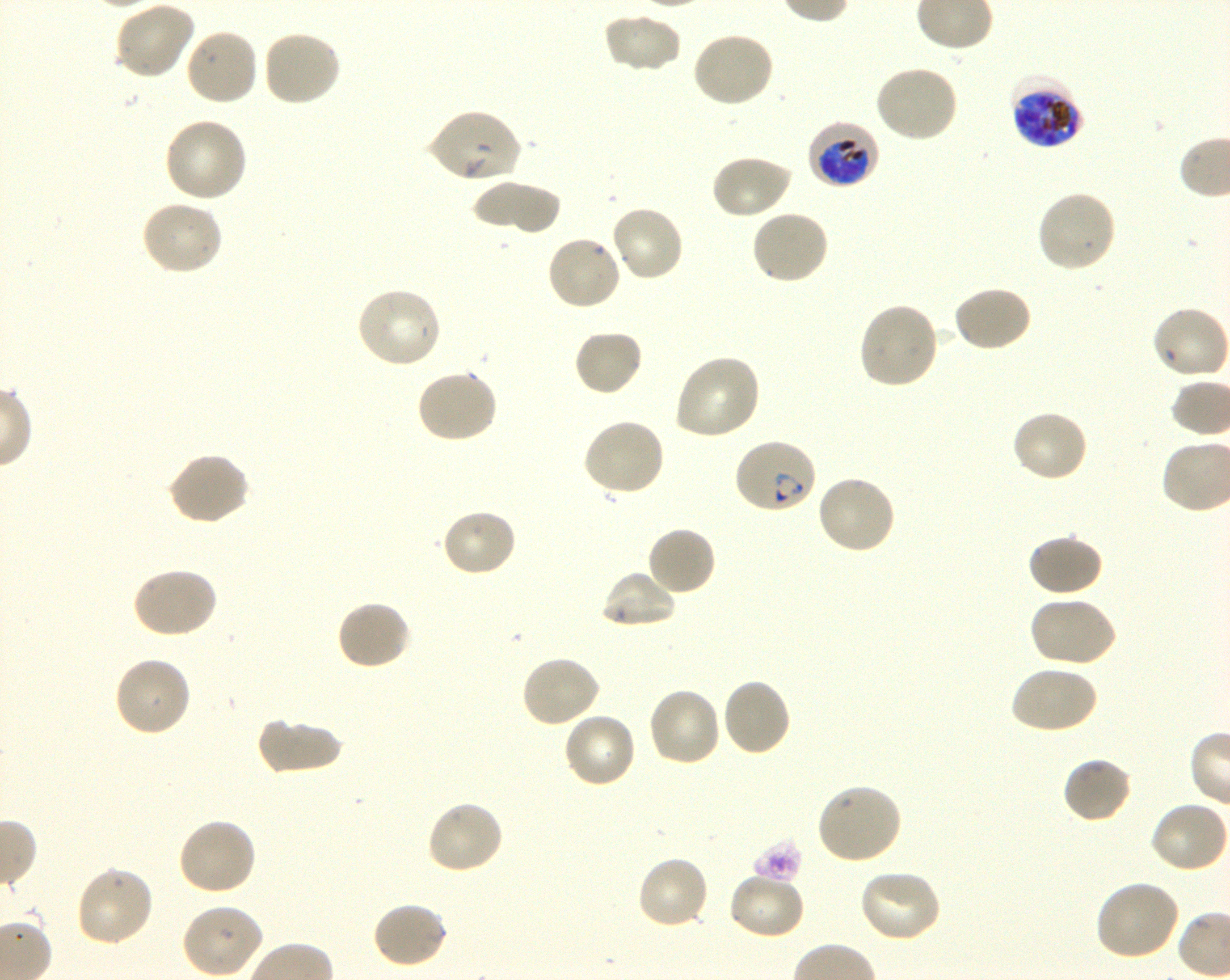

Approximate bounding boxes as [x1, y1, x2, y2] in pixels. Not every red blood cell is marked. A life-cycle stage — or a range of stages, where the recorded stages span more than one — follows each staged infected red blood cell.
Summary:
  - Locations of red blood cells of indeterminate infection status: [426, 109, 522, 185]
  - Locations of uninfected red blood cells: [113, 1, 195, 81], [602, 12, 682, 74], [183, 27, 259, 107], [261, 28, 342, 108], [690, 31, 775, 109], [873, 63, 959, 143], [164, 117, 249, 203], [709, 153, 792, 220], [470, 181, 562, 234], [1035, 188, 1118, 275], [139, 199, 224, 276], [609, 204, 685, 283], [750, 209, 830, 285], [545, 233, 623, 312], [952, 284, 1033, 353], [354, 286, 444, 369], [856, 301, 939, 391], [1150, 305, 1229, 381], [573, 328, 644, 397], [673, 353, 762, 441], [415, 368, 498, 444], [1011, 409, 1089, 484], [581, 417, 666, 497], [167, 452, 252, 527], [816, 473, 898, 555], [440, 508, 518, 579], [645, 525, 717, 597], [1026, 533, 1104, 598], [131, 566, 219, 639], [601, 569, 678, 629], [1028, 595, 1118, 668], [335, 599, 413, 670], [520, 654, 601, 729], [113, 655, 193, 738], [1009, 664, 1099, 735], [720, 677, 792, 757], [645, 686, 721, 769], [563, 710, 638, 789], [256, 717, 341, 776], [1062, 755, 1134, 824], [814, 782, 903, 866], [425, 799, 505, 876], [1149, 799, 1229, 874], [176, 817, 258, 897], [635, 855, 710, 931], [74, 864, 155, 947], [857, 869, 944, 943], [727, 871, 806, 940], [1093, 879, 1182, 962], [370, 901, 449, 969], [180, 902, 264, 977]
  - Locations of infected red blood cells: [1008, 74, 1084, 150] late trophozoite to late schizont; [807, 120, 881, 190] early trophozoite to early schizont; [733, 436, 818, 514] ring
  - Image size: 1230×980 pixels
  - Objective: 100x, oil immersion, numerical aperture 1.30
  - Preparation: thin blood film
  - Field of view: one from this slide
  - Donor blood group: O+
  - Stain: Giemsa
  - Culture: P. falciparum strain 3D7, shaking, in vitro